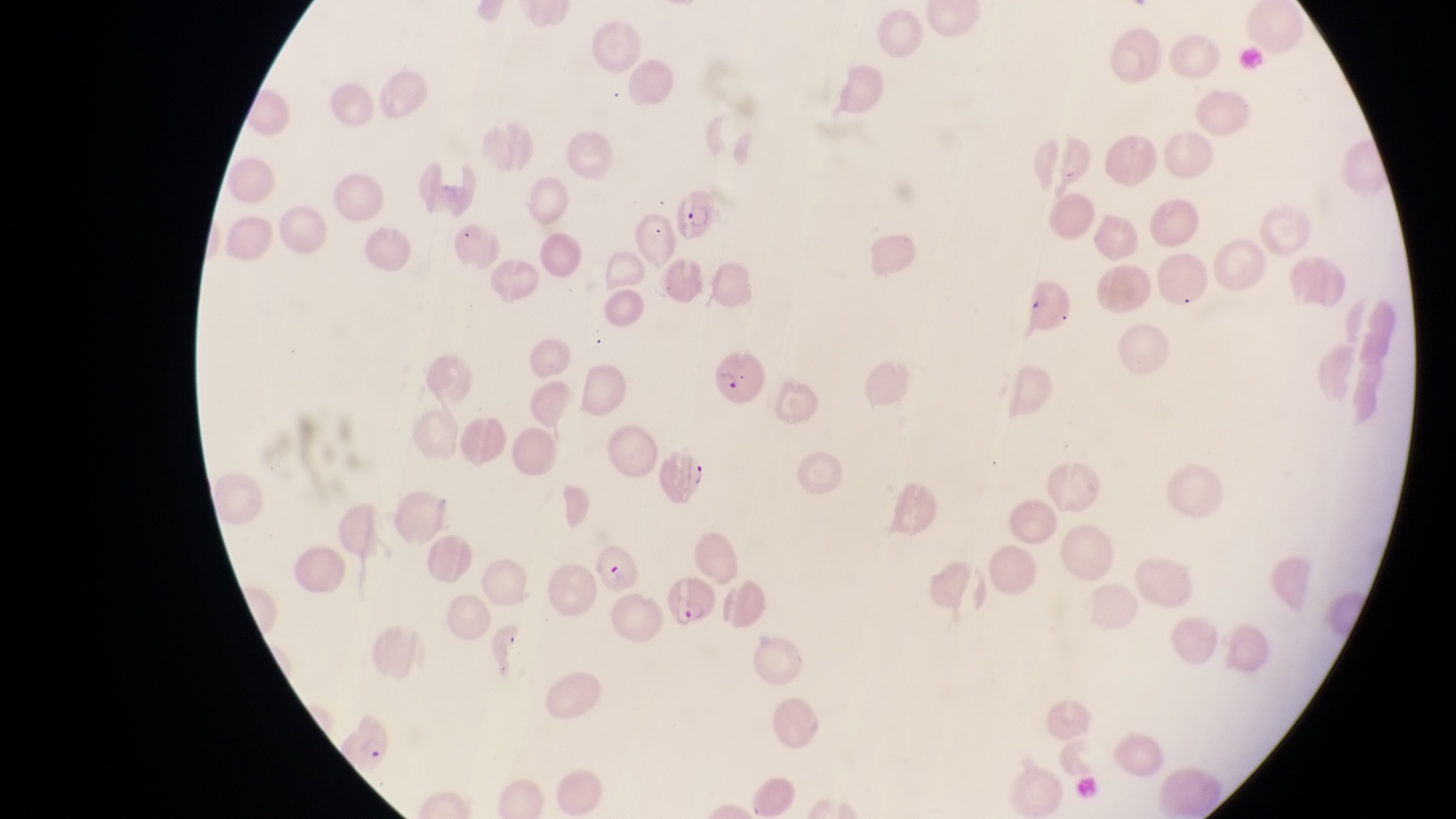

capture = smartphone photograph through the eyepiece of an Olympus CX-23 microscope
country = Uganda
preparation = thin blood film
image size = 1456×819 pixels
field of view = single
parasitised red blood cell locations = approximate bounding boxes as (left, top, right, bottom) in pixels: (676, 191, 725, 241), (714, 354, 767, 406), (658, 447, 707, 508), (591, 541, 646, 597), (668, 576, 720, 625), (343, 708, 401, 772)
magnification = 1000x